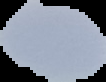
Summary:
  - Image type: cell region segmented out of the field of view; surrounding area masked to black
  - Preparation: thin blood smear
  - Malaria status: uninfected
  - Image size: 106×82 pixels